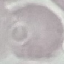

Summary:
  - Malaria status: uninfected
  - Image type: automatically extracted cell patch, resized to 64 × 64 pixels
  - Preparation: thin blood smear
  - Capture: smartphone through the microscope eyepiece
  - Stain: Giemsa